Point out each Plasmodium parasite.
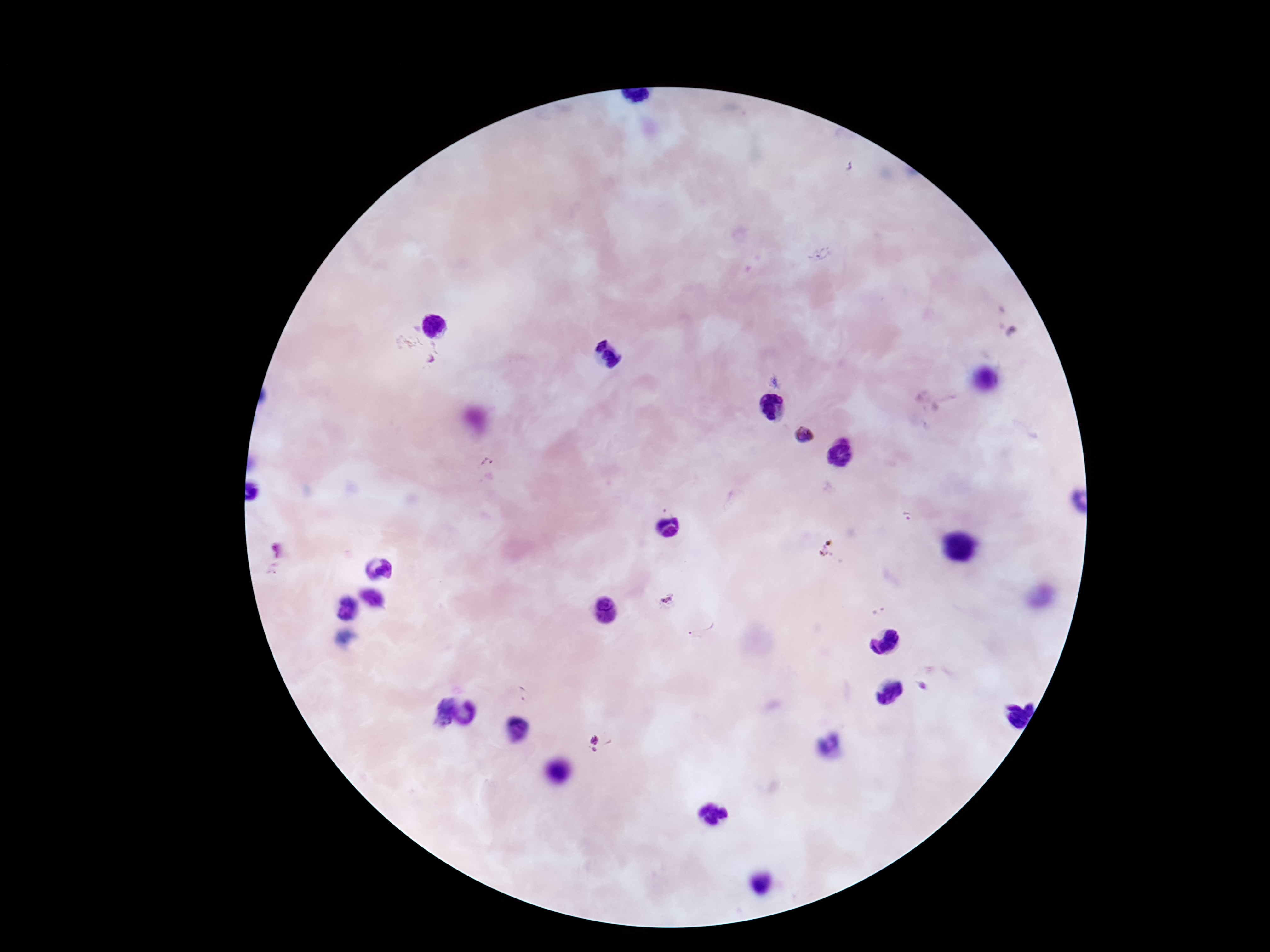
Approximate object centers, in pixels from the top-left corner.
Plasmodium parasites: (x=819, y=255), (x=408, y=343), (x=437, y=354), (x=803, y=435), (x=486, y=461), (x=907, y=517), (x=274, y=569), (x=666, y=600), (x=879, y=611), (x=702, y=625), (x=921, y=687), (x=525, y=695), (x=602, y=743).

Image is 1270×952 pixels. Patient malaria status: infected. Photographed through the microscope eyepiece with a smartphone camera. One field from this slide. Thick peripheral-blood smear. 100x magnification. Giemsa stain.